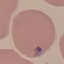

Summary:
  - Malaria status: uninfected
  - Stain: Giemsa
  - Capture: smartphone camera at the microscope eyepiece
  - Image type: automatically extracted cell patch, resized to 64 × 64 pixels
  - Preparation: thin blood film